Locate every uninfected red blood cell.
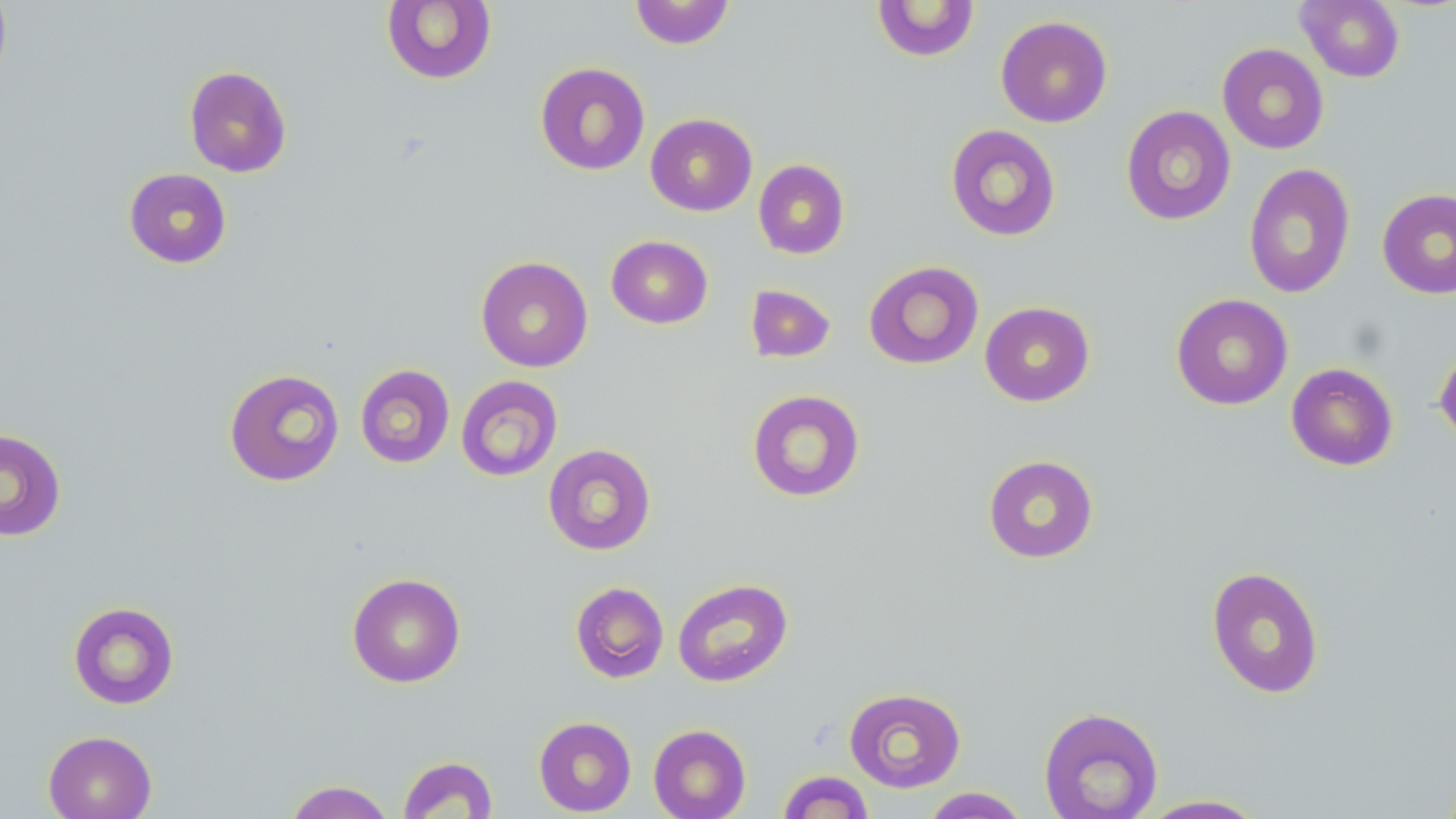

Approximate bounding boxes as named x1/y1/x2/y2 corners in pixels.
Uninfected red blood cells: (x1=0, y1=0, x2=12, y2=93), (x1=629, y1=0, x2=735, y2=49), (x1=1296, y1=0, x2=1405, y2=82), (x1=381, y1=1, x2=497, y2=85), (x1=872, y1=1, x2=980, y2=62), (x1=995, y1=15, x2=1113, y2=127), (x1=1217, y1=43, x2=1329, y2=154), (x1=535, y1=62, x2=650, y2=175), (x1=183, y1=65, x2=292, y2=177), (x1=1120, y1=105, x2=1236, y2=226), (x1=645, y1=113, x2=757, y2=216), (x1=945, y1=124, x2=1062, y2=242), (x1=753, y1=159, x2=850, y2=260), (x1=1243, y1=163, x2=1356, y2=300), (x1=124, y1=167, x2=232, y2=269), (x1=1376, y1=188, x2=1456, y2=299), (x1=605, y1=235, x2=713, y2=329), (x1=476, y1=255, x2=593, y2=372), (x1=863, y1=260, x2=984, y2=370), (x1=745, y1=284, x2=836, y2=363), (x1=1171, y1=293, x2=1293, y2=410), (x1=980, y1=301, x2=1094, y2=406), (x1=1434, y1=344, x2=1456, y2=446), (x1=1285, y1=362, x2=1399, y2=471), (x1=354, y1=364, x2=455, y2=468), (x1=224, y1=368, x2=345, y2=486), (x1=456, y1=375, x2=563, y2=481), (x1=746, y1=389, x2=866, y2=502), (x1=0, y1=428, x2=67, y2=542), (x1=543, y1=443, x2=656, y2=556), (x1=983, y1=454, x2=1099, y2=563), (x1=1206, y1=566, x2=1325, y2=699), (x1=347, y1=572, x2=465, y2=688), (x1=672, y1=578, x2=793, y2=687), (x1=570, y1=581, x2=669, y2=683), (x1=68, y1=601, x2=180, y2=709), (x1=843, y1=687, x2=966, y2=792), (x1=1038, y1=706, x2=1164, y2=819), (x1=533, y1=716, x2=636, y2=816), (x1=648, y1=724, x2=751, y2=819), (x1=43, y1=730, x2=157, y2=819), (x1=397, y1=755, x2=499, y2=818), (x1=777, y1=770, x2=874, y2=819), (x1=283, y1=780, x2=397, y2=819), (x1=921, y1=787, x2=1031, y2=818), (x1=1136, y1=794, x2=1270, y2=818).

Slide-level diagnosis: no evidence of blood parasites. Image is 1456×819 pixels. Single field of view. 1000x magnification. Thin blood smear. Light microscopy. May-Grünwald-Giemsa stain.